Locate every Plasmodium malariae-infected red blood cell.
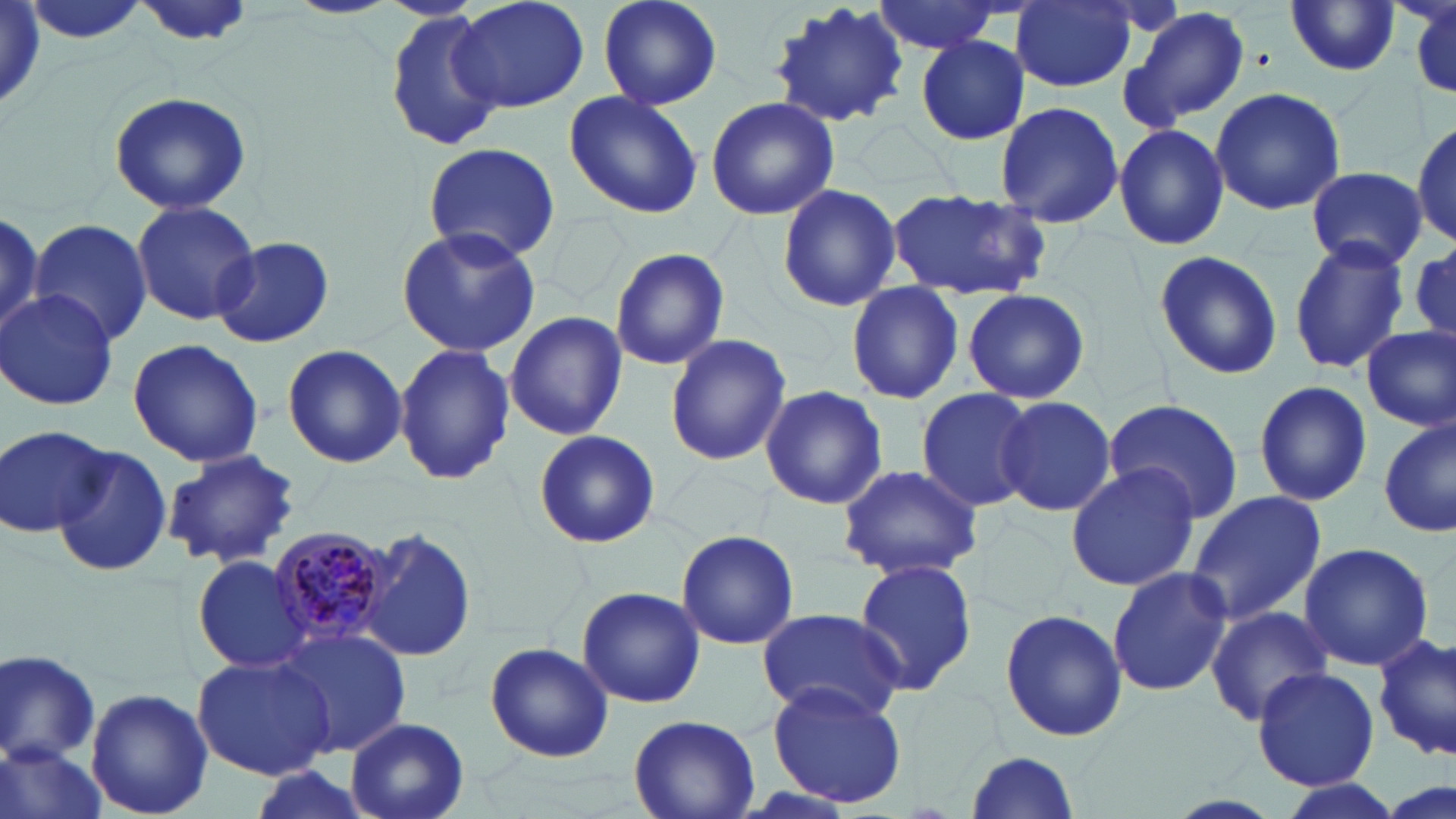
Approximate bounding boxes as (x1, y1, x2, y2) in pixels.
Plasmodium malariae-infected red blood cells: (266, 527, 396, 648).

Summary:
  - Uninfected red blood cell locations: (21, 0, 149, 47), (136, 0, 253, 49), (450, 0, 590, 113), (595, 0, 722, 114), (869, 0, 1007, 56), (1012, 0, 1137, 91), (1406, 0, 1456, 99), (1284, 3, 1402, 79), (761, 4, 940, 134), (1126, 6, 1249, 128), (383, 10, 505, 150), (915, 34, 1029, 146), (1209, 87, 1348, 214), (563, 90, 703, 218), (106, 91, 254, 215), (705, 96, 839, 221), (992, 100, 1125, 229), (1414, 117, 1455, 250), (1113, 123, 1230, 250), (421, 143, 559, 262), (1307, 168, 1427, 270), (776, 182, 902, 313), (890, 189, 1051, 302), (132, 201, 260, 325), (0, 212, 48, 338), (30, 217, 152, 346), (395, 225, 541, 357), (212, 236, 334, 349), (1289, 236, 1410, 377), (608, 246, 731, 371), (1151, 247, 1284, 381), (844, 283, 966, 405), (961, 288, 1091, 405), (0, 289, 119, 410), (505, 313, 627, 440), (1358, 328, 1454, 435), (663, 334, 792, 468), (127, 338, 265, 467), (395, 343, 514, 488), (282, 345, 408, 468), (1252, 380, 1375, 506), (760, 385, 887, 510), (914, 387, 1036, 513), (994, 396, 1120, 518), (1104, 399, 1247, 525), (1378, 417, 1455, 538), (3, 425, 113, 537), (533, 430, 659, 547), (51, 445, 174, 577), (162, 449, 303, 570), (1064, 462, 1202, 594), (835, 463, 983, 580), (1187, 488, 1326, 625), (358, 526, 475, 663), (675, 532, 800, 650), (1299, 541, 1433, 672), (192, 555, 311, 676), (851, 559, 979, 694), (1106, 566, 1232, 698), (577, 586, 705, 709), (1204, 604, 1334, 725), (755, 607, 909, 725), (998, 607, 1128, 742), (275, 627, 412, 757), (1372, 632, 1455, 761), (483, 640, 616, 762), (0, 649, 102, 766), (192, 652, 338, 779), (1252, 668, 1381, 790), (767, 681, 909, 809), (85, 687, 213, 818), (628, 714, 760, 818), (344, 716, 470, 819), (2, 744, 105, 819), (963, 749, 1082, 818), (241, 764, 375, 819), (1274, 777, 1409, 819)
  - Slide-level diagnosis: Plasmodium malariae
  - Modality: light microscopy
  - Magnification: 1000x
  - Preparation: thin blood film
  - Image size: 1456×819 pixels
  - Stain: May-Grünwald-Giemsa
  - Field of view: single